Report the malaria status of this cell.
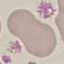

Uninfected.

Thin blood smear. Photographed with a smartphone camera at the microscope eyepiece. Giemsa-stained preparation. Cell patch, automatically extracted from a larger field of view and resized to 64 × 64 pixels.